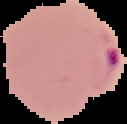

From a thin blood smear. The area outside the segmented cell region is set to black. Malaria status: parasitized. Image is 127×124 pixels.